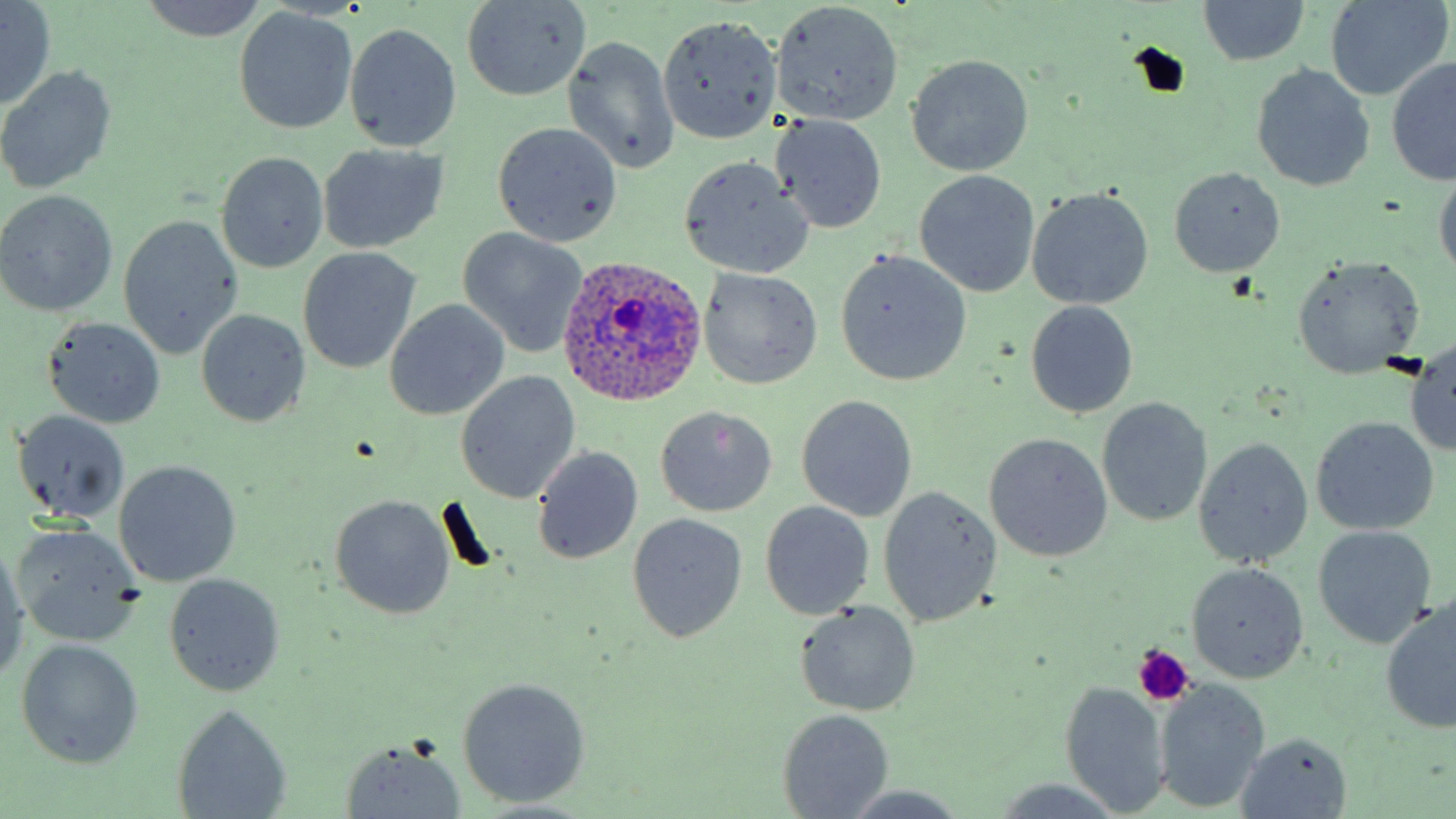

Plasmodium ovale-infected red blood cell locations = approximate bounding boxes as [x1, y1, x2, y2] in pixels: [553, 256, 709, 410]
slide-level diagnosis = Plasmodium ovale
platelet locations = approximate bounding boxes as [x1, y1, x2, y2] in pixels: [1131, 646, 1193, 704]
preparation = thin blood film
stain = May-Grünwald-Giemsa
modality = light microscopy
magnification = 1000x
uninfected red blood cell locations = approximate bounding boxes as [x1, y1, x2, y2] in pixels: [0, 0, 56, 108], [137, 0, 271, 41], [1199, 0, 1309, 68], [461, 1, 591, 101], [1323, 1, 1450, 101], [770, 2, 904, 126], [235, 10, 357, 133], [657, 15, 779, 143], [345, 23, 462, 151], [563, 35, 680, 176], [905, 54, 1035, 176], [1387, 55, 1456, 184], [0, 65, 118, 194], [1252, 65, 1375, 191], [772, 115, 887, 234], [491, 122, 622, 246], [319, 144, 448, 254], [217, 152, 329, 273], [678, 157, 813, 278], [1168, 167, 1285, 277], [1433, 170, 1456, 284], [914, 171, 1040, 298], [1027, 188, 1154, 310], [0, 190, 118, 316], [118, 215, 244, 361], [456, 228, 590, 357], [299, 249, 419, 373], [834, 250, 972, 387], [1292, 257, 1426, 377], [697, 267, 823, 390], [384, 300, 509, 420], [1024, 300, 1138, 418], [195, 309, 310, 429], [44, 317, 167, 431], [1406, 344, 1456, 457], [455, 372, 580, 505], [796, 394, 917, 522], [1097, 398, 1212, 526], [656, 406, 777, 516], [12, 410, 131, 525], [1310, 416, 1440, 536], [983, 433, 1112, 562], [1194, 436, 1314, 568], [533, 447, 643, 565], [113, 460, 242, 587], [878, 487, 1000, 626], [329, 495, 456, 621], [759, 501, 877, 618], [627, 512, 748, 644], [9, 525, 142, 647], [1311, 525, 1436, 648], [0, 541, 27, 685], [1186, 562, 1309, 683], [164, 574, 285, 696], [795, 601, 921, 717], [1379, 601, 1456, 734], [15, 639, 142, 769], [456, 677, 593, 808], [1153, 680, 1270, 812], [1059, 683, 1171, 816], [171, 704, 293, 819], [778, 709, 892, 819], [1238, 733, 1352, 816], [338, 738, 469, 818], [988, 781, 1125, 817], [838, 787, 976, 817]
field of view = one of a larger specimen
image size = 1456×819 pixels